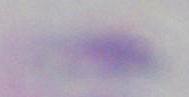

Captured at 1000x magnification. Photomicrograph. Toxoplasma gondii is seen.